Locate every blood parasite and identify its species.
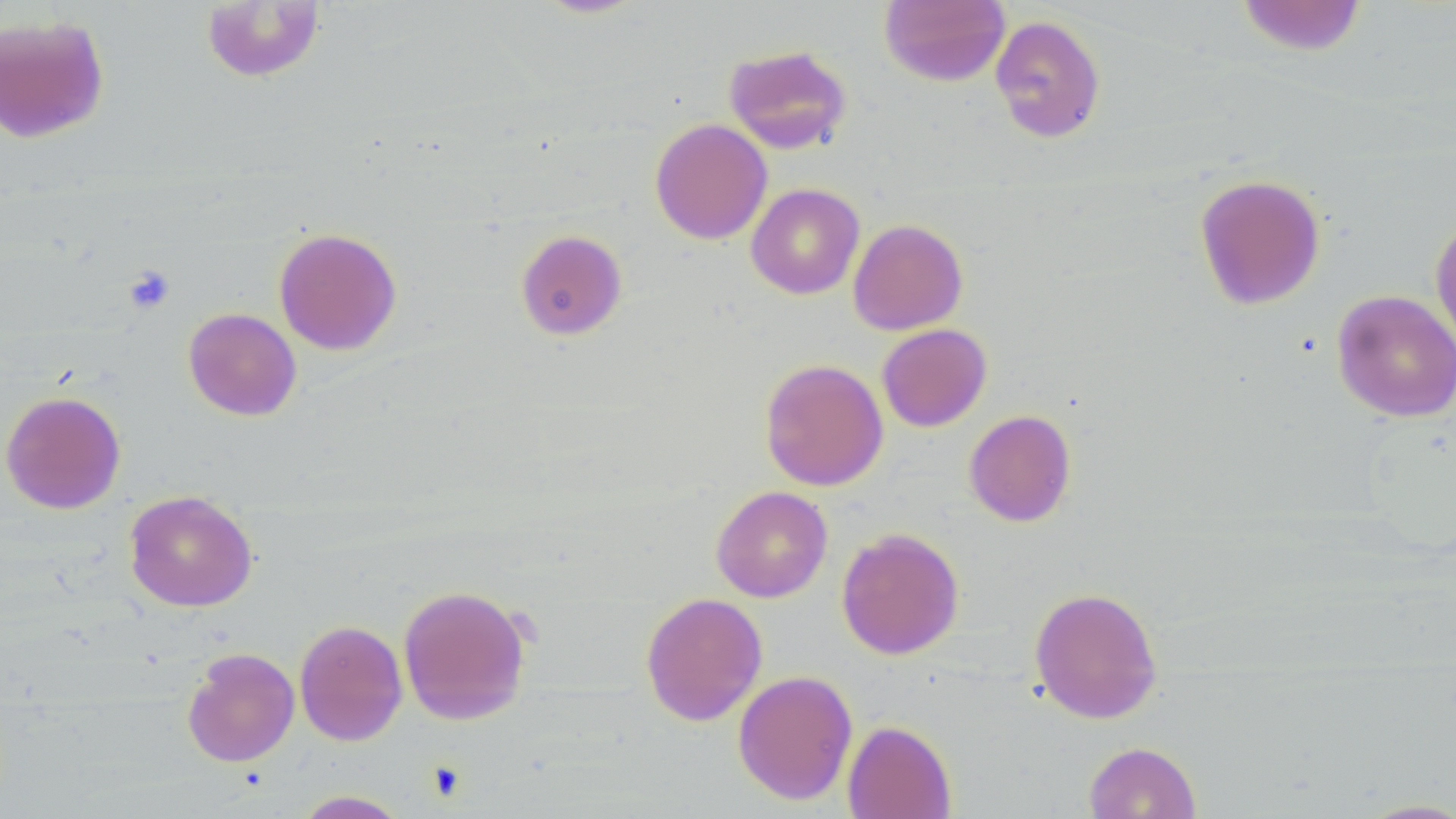

No blood parasites observed.

Summary:
  - Coordinate format: approximate bounding boxes as named x1/y1/x2/y2 corners in pixels
  - Uninfected red blood cell locations: (x1=533, y1=0, x2=648, y2=19), (x1=878, y1=0, x2=1010, y2=87), (x1=1235, y1=0, x2=1368, y2=57), (x1=201, y1=1, x2=326, y2=83), (x1=0, y1=13, x2=110, y2=143), (x1=989, y1=14, x2=1106, y2=143), (x1=723, y1=44, x2=852, y2=154), (x1=650, y1=118, x2=773, y2=245), (x1=1194, y1=173, x2=1326, y2=311), (x1=746, y1=183, x2=864, y2=299), (x1=1429, y1=212, x2=1456, y2=358), (x1=848, y1=218, x2=968, y2=335), (x1=273, y1=227, x2=402, y2=355), (x1=515, y1=229, x2=628, y2=340), (x1=1332, y1=289, x2=1456, y2=422), (x1=183, y1=307, x2=302, y2=421), (x1=877, y1=323, x2=992, y2=432), (x1=759, y1=358, x2=888, y2=491), (x1=0, y1=390, x2=126, y2=514), (x1=964, y1=409, x2=1076, y2=527), (x1=711, y1=485, x2=833, y2=603), (x1=124, y1=489, x2=257, y2=612), (x1=836, y1=527, x2=964, y2=660), (x1=397, y1=583, x2=532, y2=726), (x1=1028, y1=585, x2=1163, y2=724), (x1=640, y1=592, x2=767, y2=726), (x1=294, y1=619, x2=408, y2=746), (x1=182, y1=647, x2=300, y2=767), (x1=733, y1=670, x2=858, y2=805), (x1=841, y1=719, x2=957, y2=819), (x1=1083, y1=741, x2=1201, y2=819), (x1=292, y1=790, x2=410, y2=818), (x1=1354, y1=797, x2=1456, y2=818)
  - Platelet locations: (x1=123, y1=266, x2=175, y2=315)
  - Slide-level diagnosis: no evidence of blood parasites
  - Field of view: single
  - Preparation: thin blood smear
  - Modality: light microscopy
  - Image size: 1456×819 pixels
  - Magnification: 1000x
  - Stain: May-Grünwald-Giemsa